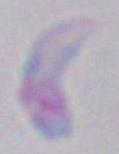

Summary:
  - Modality: photomicrograph
  - Identification: Toxoplasma gondii
  - Magnification: 1000x